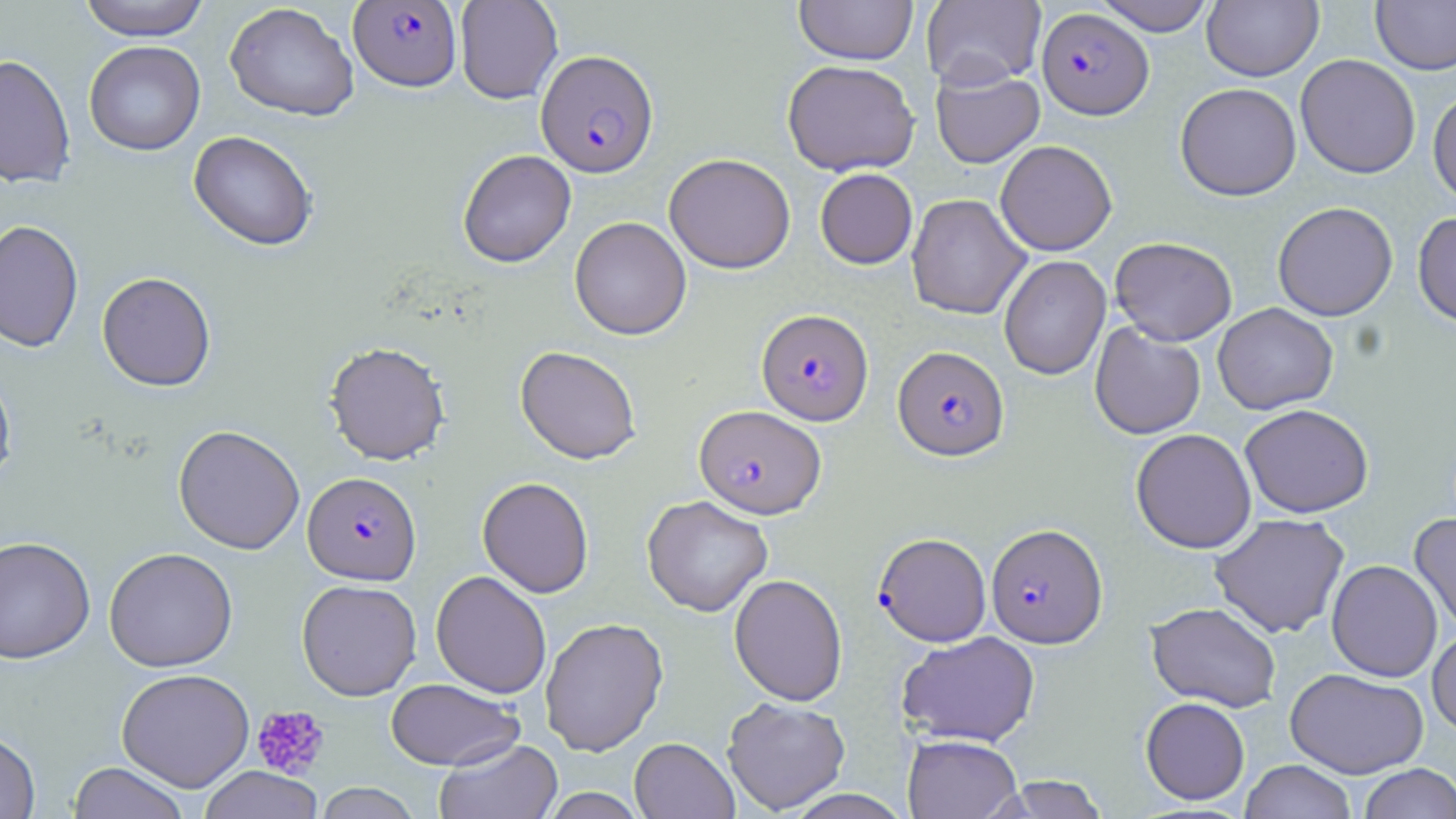
slide-level diagnosis = Plasmodium falciparum
platelet locations = approximate bounding boxes as [x1, y1, x2, y2] in pixels: [251, 704, 330, 778]
field of view = single
magnification = 1000x
stain = May-Grünwald-Giemsa
Plasmodium falciparum-infected red blood cell locations = approximate bounding boxes as [x1, y1, x2, y2] in pixels: [349, 1, 461, 92], [1037, 7, 1154, 119], [536, 49, 658, 177], [756, 308, 873, 425], [893, 345, 1009, 460], [695, 405, 826, 518], [303, 471, 421, 585], [986, 523, 1107, 648], [873, 532, 992, 646]
modality = light microscopy
preparation = thin blood smear
image size = 1456×819 pixels
uninfected red blood cell locations = approximate bounding boxes as [x1, y1, x2, y2] in pixels: [77, 0, 211, 40], [455, 0, 563, 104], [921, 0, 1046, 90], [1093, 0, 1217, 36], [1371, 0, 1456, 75], [794, 1, 918, 65], [1202, 1, 1324, 81], [224, 2, 359, 122], [83, 40, 205, 156], [0, 54, 76, 189], [1295, 54, 1421, 179], [782, 60, 920, 176], [931, 66, 1044, 168], [1175, 82, 1301, 201], [1428, 87, 1456, 206], [188, 130, 318, 251], [995, 139, 1117, 256], [457, 149, 576, 268], [664, 153, 795, 273], [815, 168, 917, 269], [906, 194, 1031, 320], [1272, 201, 1398, 321], [1413, 212, 1456, 328], [570, 216, 691, 340], [0, 219, 84, 353], [1110, 236, 1237, 345], [998, 255, 1111, 379], [97, 272, 216, 391], [1213, 303, 1338, 415], [1089, 321, 1206, 440], [324, 341, 450, 465], [515, 345, 641, 464], [0, 368, 17, 490], [1240, 404, 1373, 518], [173, 424, 305, 554], [1131, 428, 1257, 554], [477, 476, 594, 598], [642, 495, 773, 617], [1409, 512, 1456, 634], [1209, 513, 1350, 638], [0, 535, 95, 664], [104, 547, 238, 672], [1327, 559, 1442, 682], [431, 570, 551, 698], [729, 573, 848, 706], [296, 579, 422, 700], [1145, 602, 1282, 712], [540, 617, 668, 756], [1428, 627, 1456, 739], [896, 631, 1040, 747], [1285, 667, 1429, 779], [116, 668, 254, 792], [385, 678, 523, 770], [722, 697, 851, 814], [1141, 697, 1250, 805], [0, 730, 40, 818], [902, 734, 1022, 819], [433, 737, 563, 819], [629, 737, 739, 819], [1240, 760, 1357, 819], [67, 762, 189, 819], [1358, 763, 1456, 819], [199, 766, 323, 819], [995, 775, 1110, 818], [314, 783, 421, 819], [537, 787, 648, 818], [780, 789, 916, 818]